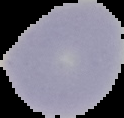

Summary:
  - Image type: segmented cell region on a black background
  - Image size: 124×118 pixels
  - Malaria status: uninfected
  - Preparation: thin blood smear